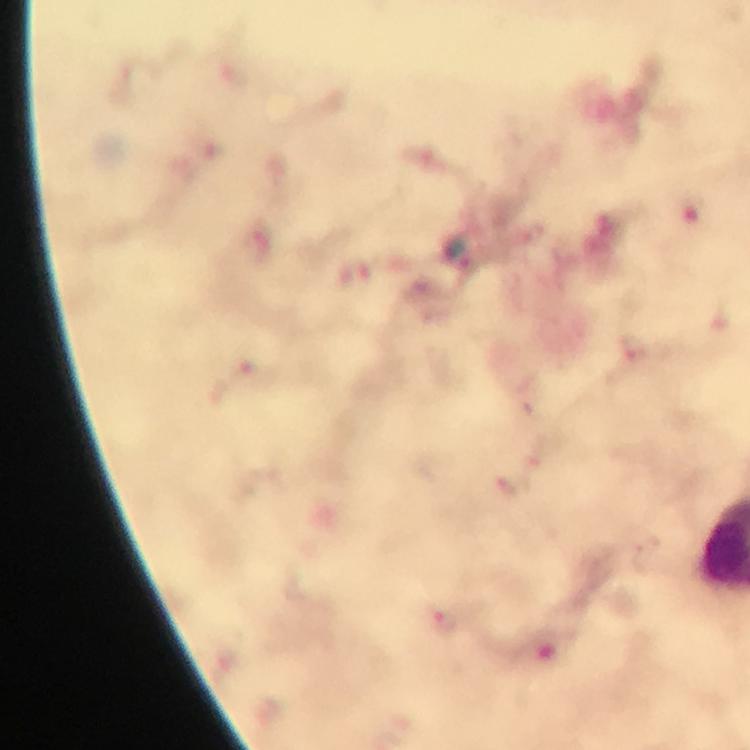
Approximate centers as {x, y} in pixels. Plasmodium parasite locations: {444, 622}. Photographed through the microscope with a smartphone camera. Thick smear. Immersion oil was used. From a diagnostic examination for malaria. Giemsa-stained preparation. At 100x magnification. Image is 750×750 pixels. A crop from one field of view.